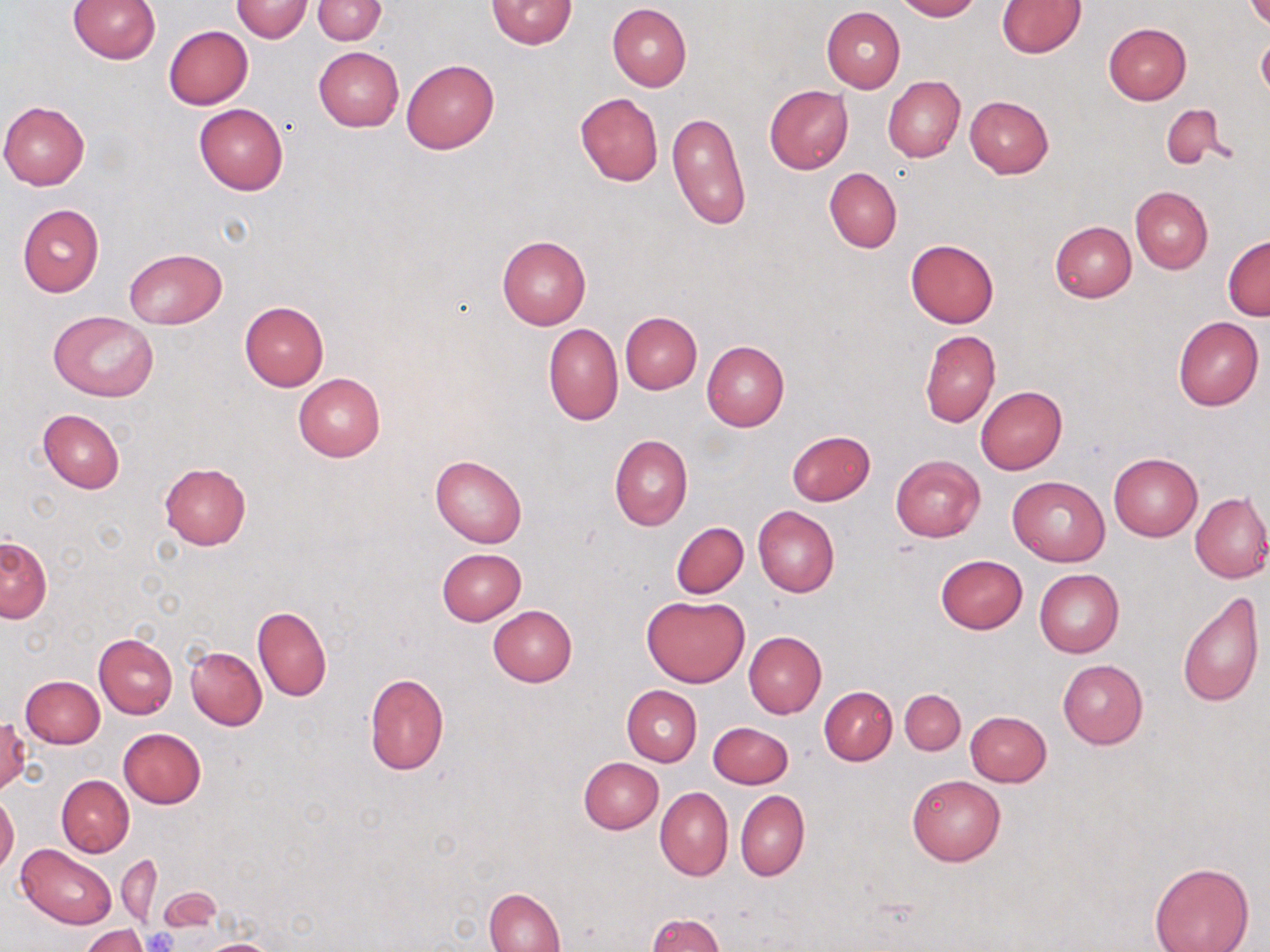

Summary:
  - Coordinate format: approximate bounding boxes as [x1, y1, x2, y2] in pixels
  - Platelet locations: [145, 927, 178, 951]
  - Uninfected red blood cell locations: [68, 0, 161, 63], [230, 0, 313, 42], [312, 0, 387, 45], [486, 0, 577, 49], [896, 0, 980, 20], [1246, 0, 1270, 30], [996, 1, 1086, 58], [607, 3, 692, 90], [822, 6, 905, 93], [1104, 22, 1191, 104], [164, 25, 253, 109], [1257, 35, 1270, 103], [313, 47, 403, 131], [401, 58, 499, 154], [883, 76, 965, 162], [765, 84, 854, 174], [575, 92, 664, 185], [964, 95, 1053, 178], [0, 101, 90, 189], [194, 104, 288, 195], [1161, 106, 1226, 170], [667, 113, 751, 230], [824, 167, 901, 252], [1130, 186, 1212, 274], [17, 204, 104, 297], [1050, 221, 1136, 302], [497, 235, 591, 329], [1223, 236, 1269, 320], [905, 239, 999, 327], [124, 248, 226, 328], [239, 301, 329, 390], [48, 310, 159, 402], [620, 312, 702, 393], [1173, 316, 1263, 411], [543, 322, 623, 426], [920, 330, 1000, 427], [702, 340, 789, 431], [292, 373, 385, 462], [975, 386, 1067, 474], [38, 409, 125, 493], [786, 430, 875, 506], [610, 434, 693, 530], [1109, 453, 1202, 541], [890, 455, 985, 542], [431, 456, 527, 547], [159, 463, 252, 550], [1007, 475, 1110, 565], [1190, 492, 1270, 583], [754, 506, 839, 597], [671, 521, 749, 599], [1, 535, 52, 622], [436, 548, 526, 625], [934, 555, 1027, 634], [1034, 569, 1124, 658], [1176, 591, 1265, 708], [641, 594, 749, 687], [488, 605, 578, 686], [253, 606, 331, 701], [743, 630, 826, 718], [93, 632, 178, 718], [186, 647, 266, 729], [1058, 660, 1148, 749], [363, 673, 448, 775], [20, 676, 104, 748], [622, 685, 702, 765], [819, 686, 897, 765], [900, 689, 965, 755], [964, 711, 1052, 787], [1, 716, 30, 794], [708, 721, 794, 789], [118, 728, 207, 809], [579, 757, 663, 833], [56, 775, 134, 856], [908, 775, 1004, 865], [655, 787, 732, 880], [735, 790, 809, 881], [0, 794, 19, 875], [18, 845, 116, 928], [117, 855, 162, 928], [1148, 862, 1255, 952], [162, 887, 221, 931], [485, 887, 565, 952], [646, 913, 725, 952], [81, 925, 148, 952], [195, 938, 281, 951]
  - Slide-level diagnosis: no evidence of blood parasites
  - Preparation: thin blood film
  - Image size: 1270×952 pixels
  - Modality: light microscopy
  - Stain: May-Grünwald-Giemsa
  - Magnification: 1000x
  - Field of view: single